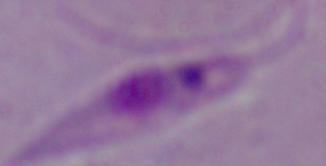

identification: Leishmania
modality: micrograph
magnification: 1000x